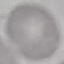
malaria status = uninfected
image type = cell patch, automatically extracted from a larger field of view and resized to 64 × 64 pixels
capture = smartphone camera at the microscope eyepiece
preparation = thin smear
stain = Giemsa